Identify the parasite.
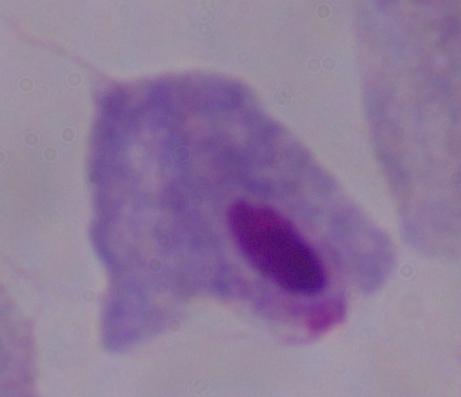

A trichomonad.

Summary:
  - Modality: micrograph
  - Magnification: 1000x